Describe the morphology of the erythrocytes.
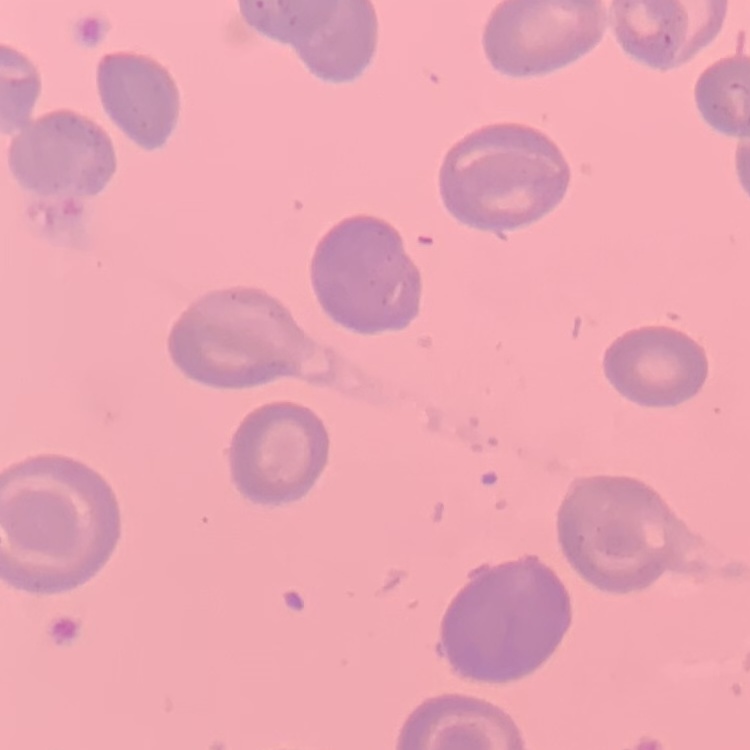
No rouleaux formation.

image_type: one tile cut from a larger photomicrograph
stain: Field's or Giemsa
preparation: thin blood smear